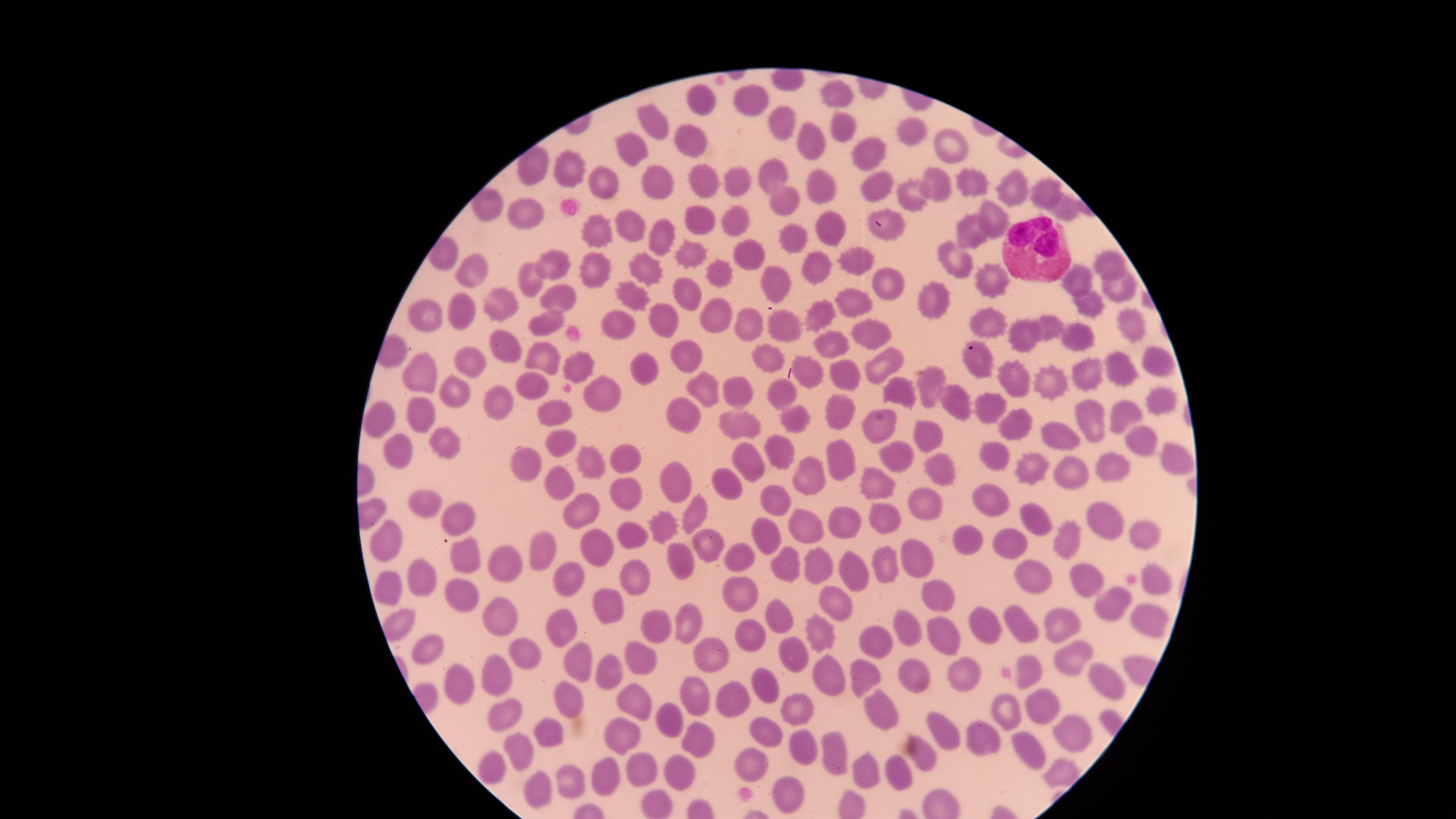 Approximate marker points as (x, y) in pixels. White blood cells: (1031, 248). Uninfected red blood cells: (836, 91), (750, 95), (701, 101), (650, 114), (774, 118), (848, 123), (915, 130), (687, 137), (814, 139), (954, 140), (633, 147), (863, 148), (564, 170), (778, 175), (707, 180), (733, 180), (937, 182), (975, 182), (657, 183), (608, 185), (820, 187), (876, 188), (1012, 190), (1048, 192), (779, 199), (912, 199), (1061, 207), (527, 210), (732, 216), (989, 218), (700, 219), (631, 225), (824, 225), (887, 230), (596, 233), (975, 234), (786, 240), (663, 243), (689, 248), (745, 251), (556, 260), (955, 260), (1105, 260), (860, 262), (640, 267), (812, 267), (466, 268), (596, 270), (719, 276), (988, 276), (884, 278), (528, 281), (774, 281), (1078, 283), (1122, 288), (683, 294), (632, 295), (549, 296), (853, 298), (934, 298), (499, 304), (459, 307), (1090, 307), (817, 309), (710, 314), (665, 317), (428, 320), (543, 321), (750, 321), (1126, 322), (616, 323), (782, 324), (989, 326), (1052, 326), (868, 328), (1026, 335), (1078, 335), (829, 340), (506, 349), (766, 353), (688, 355), (542, 356), (460, 358), (1161, 360), (976, 361), (876, 362), (577, 364), (640, 366), (812, 368), (1118, 368), (1084, 370), (839, 371), (423, 375), (930, 376), (1009, 381), (1047, 381), (898, 388), (533, 389), (705, 389), (779, 389), (451, 392), (741, 393), (601, 394), (500, 395), (953, 398), (1162, 403), (994, 404), (418, 410), (838, 410), (1126, 410), (554, 411), (685, 415), (374, 418), (800, 418), (1093, 420), (1020, 421), (738, 427), (873, 430), (924, 430), (1065, 433), (559, 437), (445, 440), (1143, 441), (777, 447), (991, 451), (394, 452), (631, 455), (1168, 456), (897, 458), (514, 459), (588, 460), (750, 462), (837, 463), (1113, 463), (1034, 466), (940, 467), (812, 474), (1066, 474), (674, 477), (729, 481), (867, 481), (558, 489), (621, 494), (987, 499), (925, 500), (423, 501), (779, 501), (578, 509), (691, 513), (1037, 515), (453, 517), (884, 518), (1107, 521), (807, 522), (844, 523), (1140, 530), (667, 531), (629, 534), (970, 536), (386, 537), (766, 537), (1068, 537), (1009, 538), (706, 543), (599, 547), (538, 550), (736, 550), (918, 553), (467, 554), (685, 557), (816, 561), (507, 564), (782, 565), (884, 567), (847, 568), (1080, 573), (630, 576), (1029, 577), (420, 578), (1160, 578), (573, 581), (389, 582), (739, 590), (459, 592), (939, 593), (839, 603), (1115, 607), (607, 609), (500, 612), (777, 619), (690, 621), (1020, 621), (1151, 621), (656, 624), (982, 624), (1055, 626), (911, 627), (561, 630), (755, 632), (947, 632), (826, 633), (871, 636), (430, 645), (714, 650), (523, 651), (793, 653), (641, 654), (1069, 656), (581, 662), (609, 667), (860, 672), (1096, 673), (961, 674), (828, 676), (1033, 676), (493, 678), (907, 679), (463, 682), (768, 688), (696, 695), (726, 699), (569, 700), (1041, 703), (637, 704), (874, 704), (794, 706), (1003, 709), (509, 715), (665, 724), (943, 728), (1069, 731), (553, 732), (771, 736), (620, 738), (986, 741), (697, 742), (520, 749), (831, 749), (811, 751), (1022, 751), (751, 756), (920, 756), (642, 765), (490, 769), (903, 769), (863, 770), (678, 771), (603, 776), (568, 782), (540, 794), (787, 794). Presence: no malaria parasites detected. Thin blood film. Photographed with a smartphone camera through the microscope eyepiece. Giemsa stain. Image is 1456×819 pixels. Circular visible region. One field of view of the specimen.